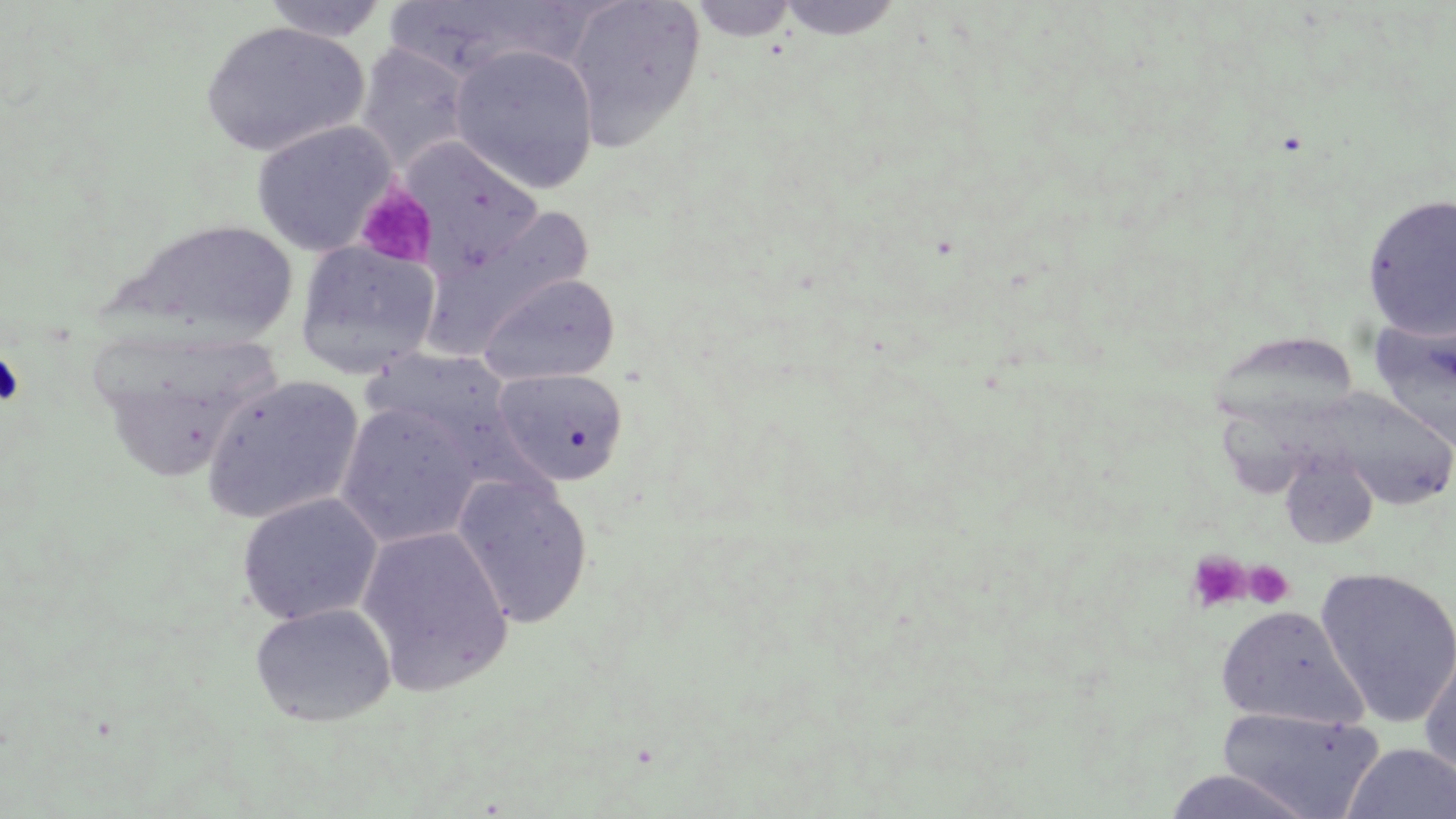
slide_level_diagnosis: negative for blood parasites
magnification: 1000x
preparation: thin blood smear
uninfected_red_blood_cell_locations: 'approximate bounding boxes as named x1/y1/x2/y2 corners in pixels: (x1=258, y1=0, x2=393, y2=43), (x1=560, y1=0, x2=706, y2=149), (x1=686, y1=0, x2=799, y2=42), (x1=775, y1=0, x2=905, y2=41), (x1=381, y1=3, x2=590, y2=84), (x1=199, y1=20, x2=370, y2=157), (x1=355, y1=43, x2=473, y2=175), (x1=449, y1=44, x2=601, y2=194), (x1=250, y1=120, x2=398, y2=256), (x1=402, y1=140, x2=546, y2=272), (x1=1362, y1=193, x2=1456, y2=338), (x1=422, y1=208, x2=595, y2=354), (x1=119, y1=218, x2=301, y2=345), (x1=294, y1=240, x2=442, y2=379), (x1=477, y1=273, x2=620, y2=385), (x1=1370, y1=314, x2=1456, y2=453), (x1=492, y1=367, x2=630, y2=487), (x1=201, y1=375, x2=365, y2=525), (x1=1308, y1=387, x2=1454, y2=511), (x1=335, y1=402, x2=482, y2=548), (x1=1279, y1=454, x2=1379, y2=550), (x1=451, y1=472, x2=593, y2=629), (x1=235, y1=492, x2=383, y2=627), (x1=356, y1=525, x2=514, y2=696), (x1=1315, y1=566, x2=1456, y2=727), (x1=250, y1=602, x2=396, y2=728), (x1=1215, y1=604, x2=1363, y2=727), (x1=1418, y1=635, x2=1456, y2=780), (x1=1218, y1=707, x2=1385, y2=817), (x1=1343, y1=743, x2=1456, y2=818), (x1=1161, y1=769, x2=1322, y2=819)'
stain: May-Grünwald-Giemsa
image_size: 1456×819 pixels
field_of_view: single
platelet_locations: 'approximate bounding boxes as named x1/y1/x2/y2 corners in pixels: (x1=354, y1=181, x2=438, y2=270), (x1=0, y1=349, x2=26, y2=408), (x1=1186, y1=550, x2=1252, y2=613), (x1=1243, y1=562, x2=1294, y2=608)'
modality: optical microscopy